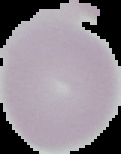 Malaria status: uninfected. The area outside the segmented cell region is set to black. Image is 121×154 pixels. From a thin blood smear.